Assess the morphology of the red blood cells.
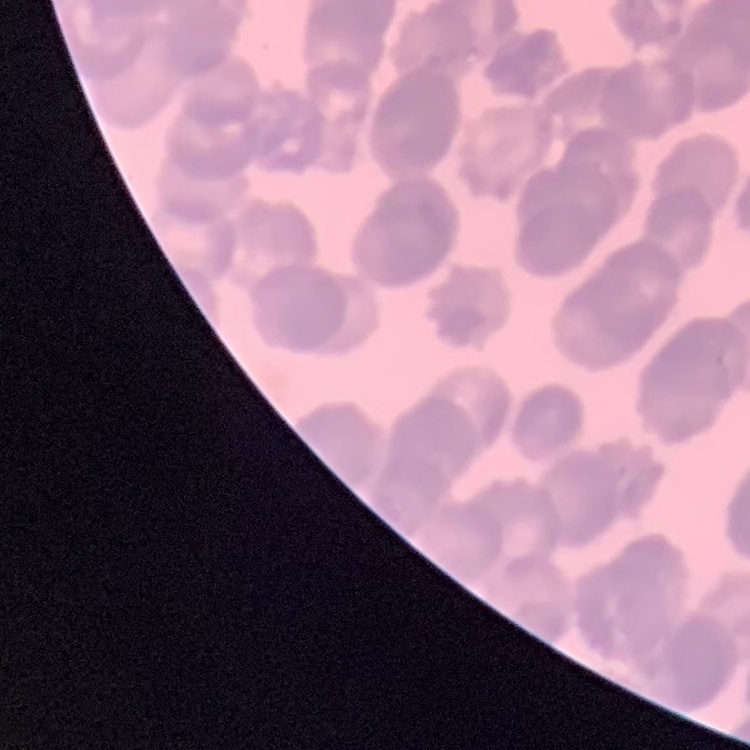

Rouleaux formation.

Summary:
  - Stain: Field's or Giemsa
  - Image type: square crop of a larger photomicrograph
  - Preparation: thin blood film